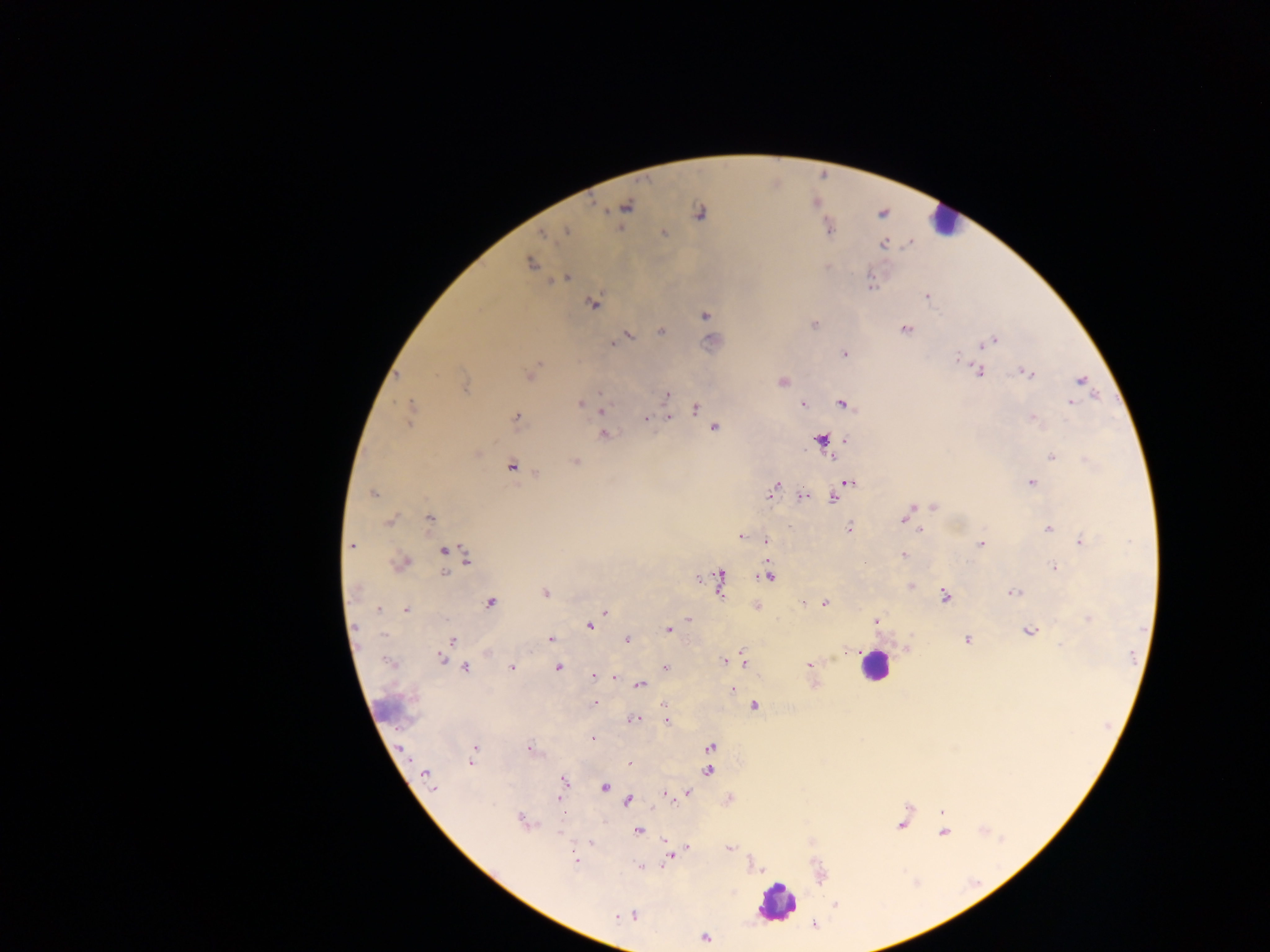

Approximate centers as [x, y] in pixels.
Summary:
  - Leukocyte locations: [942, 221], [874, 665], [389, 707], [775, 902]
  - Malaria parasite locations: [626, 207], [699, 212], [565, 231], [664, 233], [544, 234], [883, 244], [530, 263], [565, 278], [870, 283], [927, 296], [593, 305], [704, 316], [814, 325], [905, 330], [661, 332], [628, 336], [621, 340], [994, 340], [613, 342], [983, 344], [844, 353], [957, 357], [980, 371], [1028, 373], [529, 375], [782, 381], [1082, 381], [464, 385], [599, 394], [667, 395], [1070, 403], [580, 404], [802, 404], [844, 404], [695, 408], [410, 410], [602, 410], [516, 417], [669, 418], [645, 419], [1034, 419], [714, 428], [604, 434], [821, 439], [846, 440], [477, 454], [1052, 457], [1088, 461], [575, 462], [512, 466], [849, 482], [1031, 482], [776, 487], [373, 494], [802, 497], [833, 498], [934, 507], [911, 509], [429, 518], [902, 520], [390, 522], [849, 528], [920, 529], [1048, 529], [740, 537], [766, 541], [1081, 541], [981, 544], [351, 546], [444, 550], [903, 555], [465, 557], [399, 563], [1054, 568], [444, 573], [768, 576], [719, 581], [910, 586], [356, 589], [1014, 592], [545, 593], [945, 595], [491, 603], [803, 603], [825, 603], [379, 609], [405, 610], [605, 612], [689, 619], [1088, 619], [876, 620], [589, 626], [669, 630], [1029, 631], [383, 635], [552, 639], [967, 639], [626, 640], [452, 641], [849, 652], [440, 658], [743, 660], [724, 661], [730, 661], [808, 665], [511, 667], [665, 667], [466, 668], [558, 668], [593, 676], [614, 677], [640, 685], [732, 690], [594, 704], [754, 706], [664, 707], [635, 719], [667, 720], [594, 738], [711, 746], [474, 749], [529, 749], [471, 761], [629, 764], [708, 771], [426, 774], [564, 781], [563, 785], [432, 787], [605, 787], [687, 792], [665, 794], [559, 800], [628, 801], [520, 820], [901, 823], [638, 831], [943, 832], [590, 842], [688, 848], [729, 848], [670, 855], [575, 860], [641, 866], [836, 904], [633, 915], [617, 917], [705, 937]
  - Image size: 1270×952 pixels
  - Preparation: thick blood film
  - Capture: mobile-phone photograph through a microscope
  - Field of view: single
  - Country: Ghana